Locate and identify every blood parasite.
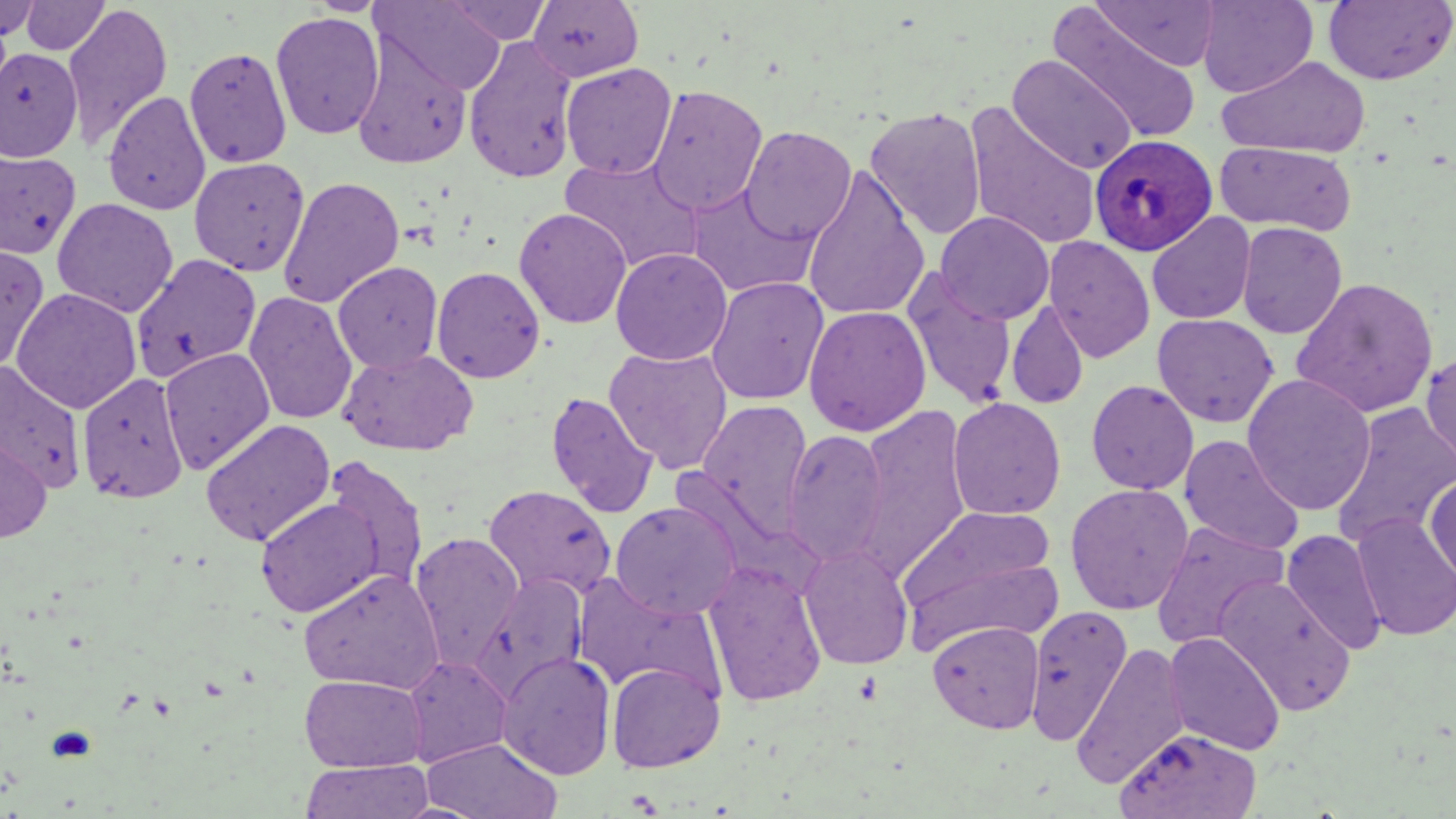
Approximate bounding boxes as [x1, y1, x2, y2] in pixels.
Plasmodium ovale-infected red blood cells: [1090, 135, 1216, 255].
No Plasmodium falciparum, Plasmodium malariae, Plasmodium vivax, Babesia divergens, or Trypanosoma brucei observed.

{
  "slide_level_diagnosis": "Plasmodium ovale",
  "modality": "optical microscopy",
  "field_of_view": "single",
  "preparation": "thin blood film",
  "stain": "May-Grünwald-Giemsa",
  "magnification": "1000x",
  "uninfected_red_blood_cell_locations": "approximate bounding boxes as [x1, y1, x2, y2] in pixels: [20, 0, 109, 55], [445, 0, 551, 44], [528, 0, 644, 82], [1197, 0, 1318, 98], [1323, 0, 1456, 86], [0, 1, 41, 41], [375, 1, 507, 95], [1092, 1, 1220, 71], [61, 2, 174, 152], [1049, 5, 1203, 145], [270, 11, 385, 140], [352, 36, 472, 169], [463, 36, 578, 183], [184, 46, 293, 168], [0, 48, 82, 162], [1007, 54, 1138, 175], [1220, 55, 1370, 160], [561, 62, 677, 179], [647, 85, 768, 215], [102, 90, 212, 215], [964, 103, 1102, 252], [865, 106, 986, 240], [739, 125, 857, 245], [1215, 141, 1357, 236], [0, 149, 81, 260], [189, 156, 311, 276], [559, 156, 704, 273], [801, 164, 930, 323], [277, 175, 404, 309], [687, 187, 816, 298], [52, 197, 178, 317], [513, 207, 632, 328], [935, 211, 1055, 324], [1147, 213, 1256, 324], [1236, 222, 1347, 339], [1042, 235, 1156, 363], [0, 243, 48, 374], [611, 247, 731, 365], [131, 253, 262, 382], [332, 261, 443, 374], [431, 266, 545, 383], [901, 271, 1017, 409], [706, 276, 829, 404], [1291, 277, 1439, 417], [11, 287, 142, 413], [243, 290, 358, 425], [1005, 298, 1089, 410], [804, 304, 931, 437], [1152, 313, 1279, 428], [604, 346, 733, 475], [159, 347, 275, 474], [338, 348, 479, 456], [1421, 348, 1456, 476], [0, 360, 88, 493], [77, 372, 190, 504], [1242, 373, 1376, 514], [1086, 379, 1198, 495], [546, 390, 659, 518], [947, 397, 1067, 520], [696, 400, 813, 532], [1331, 402, 1455, 551], [853, 403, 973, 577], [200, 418, 336, 546], [781, 427, 890, 568], [0, 433, 53, 544], [1180, 434, 1305, 556], [323, 456, 429, 592], [1424, 472, 1456, 585], [482, 483, 616, 599], [1065, 483, 1194, 615], [254, 499, 381, 618], [609, 500, 742, 619], [899, 507, 1062, 645], [1350, 513, 1456, 641], [1150, 521, 1289, 650], [1281, 529, 1387, 655], [409, 531, 524, 671], [798, 542, 915, 670], [703, 560, 827, 707], [298, 569, 445, 694], [472, 573, 587, 701], [572, 573, 724, 700], [1216, 576, 1357, 714], [1025, 604, 1133, 746], [928, 621, 1045, 733], [1164, 631, 1286, 756], [1072, 642, 1190, 788], [497, 651, 616, 780], [402, 655, 512, 767], [607, 661, 724, 773], [299, 673, 428, 772], [1116, 728, 1262, 819], [421, 736, 562, 818], [301, 759, 434, 819]",
  "image_size": "1456×819 pixels"
}